Locate every blood parasite and identify its species.
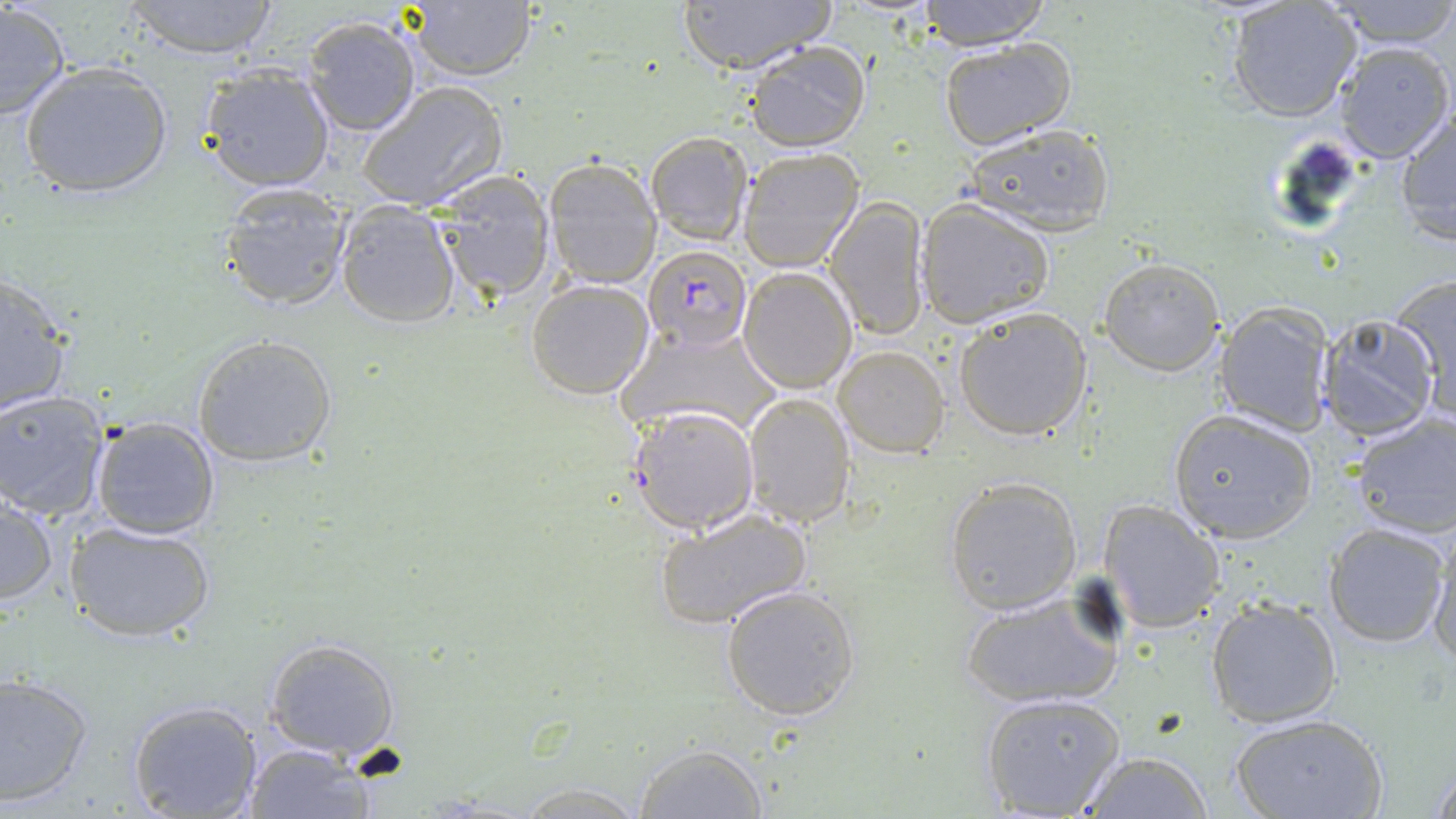

Approximate bounding boxes as (x1,y1)-(x2,y2) corner pairs in pixels.
Plasmodium falciparum-infected red blood cells: (644,244)-(751,350), (627,404)-(759,535).
No Plasmodium ovale, Plasmodium malariae, Plasmodium vivax, Babesia divergens, or Trypanosoma brucei observed.

Summary:
  - Uninfected red blood cell locations: (121,0)-(283,60), (400,0)-(538,83), (676,0)-(835,74), (913,0)-(1053,48), (1327,0)-(1456,51), (0,2)-(71,121), (1227,2)-(1363,123), (301,16)-(424,138), (938,38)-(1075,147), (745,40)-(869,152), (1331,41)-(1454,164), (18,61)-(173,200), (197,63)-(336,193), (356,80)-(508,213), (1393,106)-(1455,246), (961,124)-(1116,236), (645,131)-(753,247), (737,147)-(864,271), (543,156)-(663,289), (432,170)-(555,304), (218,181)-(352,312), (825,197)-(931,342), (333,198)-(460,327), (915,200)-(1055,328), (1096,256)-(1225,376), (737,265)-(857,393), (0,270)-(73,418), (1387,275)-(1456,406), (524,279)-(655,401), (1213,302)-(1335,436), (952,306)-(1093,442), (1316,315)-(1441,442), (620,323)-(781,440), (192,333)-(339,468), (832,345)-(950,457), (0,390)-(110,520), (742,392)-(857,528), (1167,408)-(1319,541), (1348,412)-(1456,539), (88,414)-(221,539), (943,476)-(1083,615), (0,497)-(58,605), (1098,498)-(1225,633), (655,509)-(813,631), (64,519)-(216,643), (1322,521)-(1451,647), (1428,529)-(1456,669), (719,583)-(862,722), (960,588)-(1125,709), (1207,596)-(1342,728), (261,636)-(402,759), (0,670)-(94,805), (980,693)-(1125,817), (127,699)-(263,818), (1230,712)-(1386,819), (243,741)-(375,818), (633,741)-(768,818), (1079,750)-(1214,819), (1429,756)-(1456,818), (504,780)-(656,817)
  - Slide-level diagnosis: Plasmodium falciparum
  - Field of view: one of a larger specimen
  - Magnification: 1000x
  - Stain: May-Grünwald-Giemsa
  - Modality: light microscopy
  - Image size: 1456×819 pixels
  - Preparation: thin blood smear